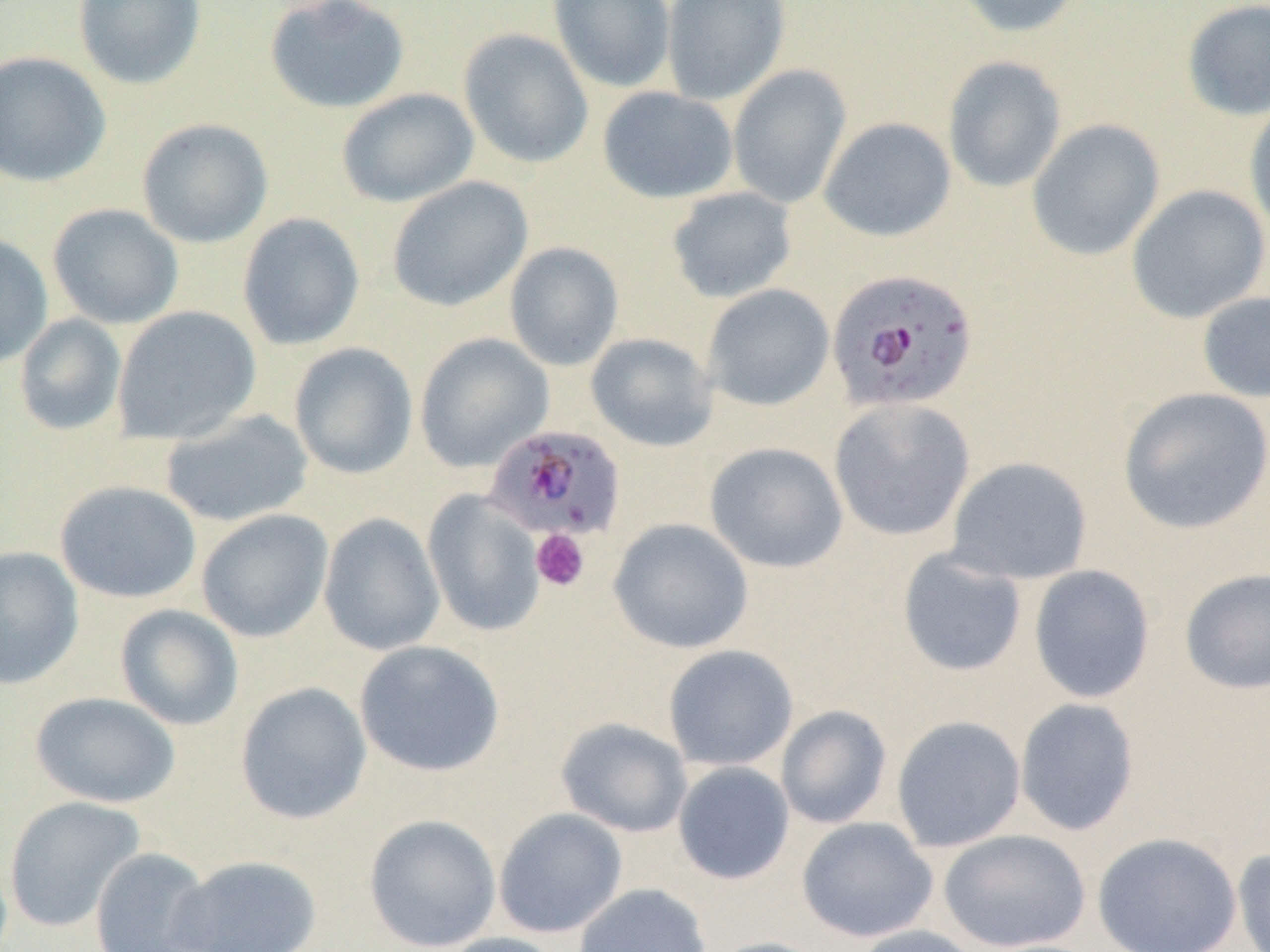
Plasmodium falciparum-infected red blood cell locations = approximate bounding boxes as (x1,y1)-(x2,y2) corner pairs in pixels: (826,268)-(979,414), (486,423)-(627,540)
slide-level diagnosis = Plasmodium falciparum
magnification = 1000x
image size = 1270×952 pixels
uninfected red blood cell locations = approximate bounding boxes as (x1,y1)-(x2,y2) corner pairs in pixels: (72,0)-(207,90), (264,0)-(410,114), (548,0)-(676,93), (661,0)-(791,105), (951,0)-(1085,38), (1182,1)-(1269,121), (458,28)-(593,168), (0,50)-(111,188), (942,56)-(1066,193), (727,64)-(852,209), (597,86)-(739,204), (336,88)-(478,207), (1244,99)-(1270,238), (819,117)-(956,242), (136,118)-(274,248), (1027,119)-(1165,261), (386,176)-(533,312), (1126,184)-(1270,324), (667,187)-(797,303), (47,203)-(184,329), (237,212)-(365,351), (0,233)-(54,369), (504,241)-(624,371), (701,284)-(834,411), (1197,291)-(1270,403), (112,306)-(261,445), (14,313)-(127,436), (586,332)-(718,451), (414,333)-(553,472), (289,342)-(418,479), (1117,387)-(1270,535), (828,398)-(976,541), (159,409)-(314,527), (704,441)-(848,573), (946,456)-(1094,585), (54,480)-(202,603), (422,490)-(545,638), (196,509)-(333,642), (318,513)-(445,655), (608,517)-(753,653), (0,546)-(84,689), (896,548)-(1028,677), (1028,564)-(1155,703), (1179,567)-(1270,695), (115,604)-(244,731), (354,640)-(505,777), (663,644)-(799,771), (234,681)-(372,825), (29,691)-(181,808), (1014,697)-(1139,836), (776,705)-(892,829), (891,715)-(1026,852), (555,717)-(693,838), (672,761)-(795,885), (3,796)-(146,933), (493,808)-(628,939), (363,814)-(502,951), (796,816)-(938,942), (937,829)-(1090,952), (1092,831)-(1242,952), (89,847)-(217,952), (1232,847)-(1270,952), (170,854)-(322,951), (573,883)-(711,952), (850,925)-(985,952), (434,932)-(569,952), (705,936)-(835,952)
platelet locations = approximate bounding boxes as (x1,y1)-(x2,y2) corner pairs in pixels: (530,529)-(590,591)
field of view = one of a larger specimen
modality = optical microscopy
preparation = thin blood smear